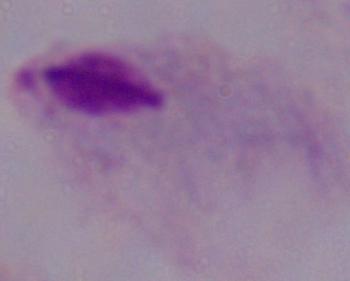
Summary:
  - Modality: micrograph
  - Identification: trichomonad
  - Magnification: 1000x